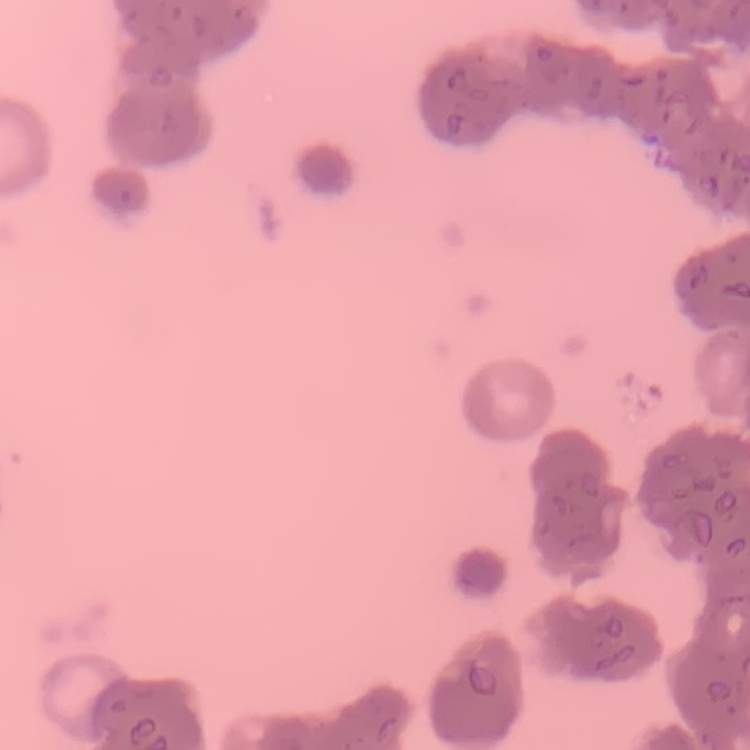
The red blood cells exhibit rouleaux formation. Field's or Giemsa stain. One tile cut from a larger photomicrograph. Thin peripheral smear.